Locate every malaria parasite.
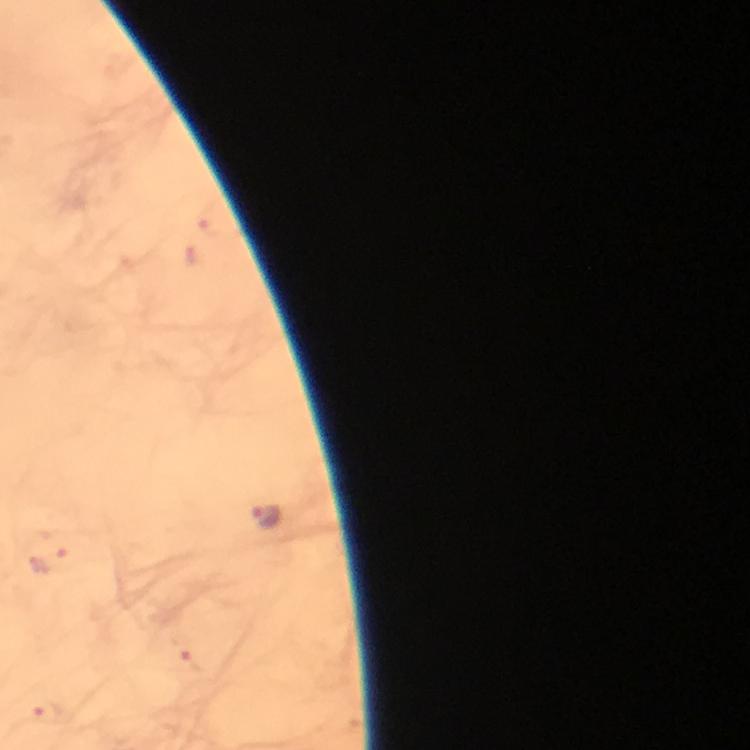

Approximate centers as [x, y] in pixels.
Malaria parasites: [267, 516], [49, 560], [187, 661], [47, 715].

stain = Giemsa
image size = 750×750 pixels
capture = smartphone camera through the microscope
context = from a diagnostic examination for malaria
cropped from = a single field of view
preparation = thick blood film
immersion oil = applied
magnification = 100x